Comment on the morphology of the red blood cells.
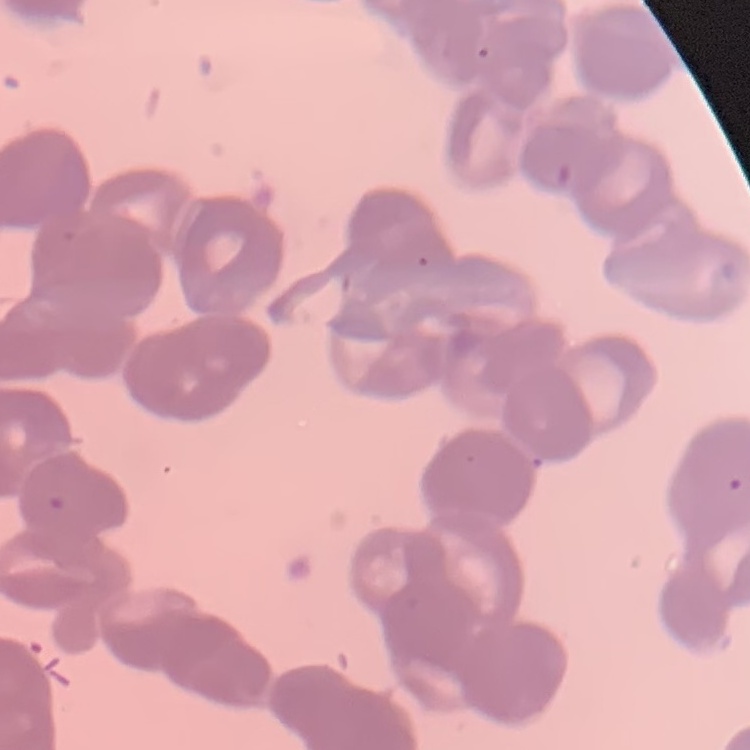
They show rouleaux formation.

Summary:
  - Preparation: thin blood smear
  - Image type: one tile cut from a larger photomicrograph
  - Stain: Field's or Giemsa